Assess this cell for malaria.
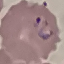
It is parasitized.

Automatically extracted cell patch, resized to 64 × 64 pixels. Thin blood film. Photographed with a smartphone camera at the microscope eyepiece. Giemsa-stained preparation.